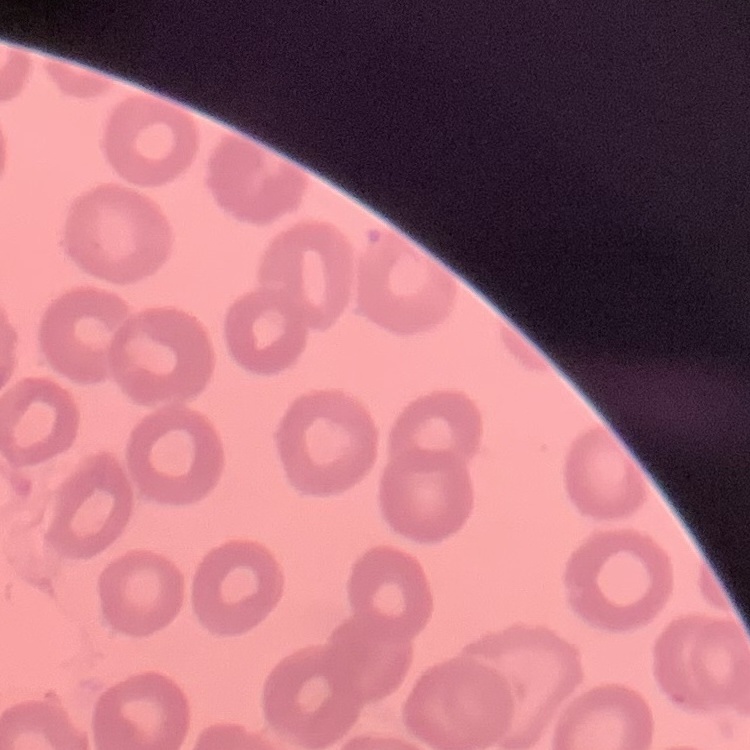

The red blood cells show no rouleaux formation. Thin blood film. Field's or Giemsa stain. One tile cut from a larger photomicrograph.